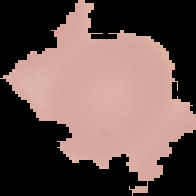

preparation: thin blood smear
image_type: segmented cell region with the area outside set to black
image_size: 196×196 pixels
result: negative for malaria parasites